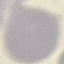
Summary:
  - Result: no malaria parasites detected
  - Image type: cell patch, automatically extracted from a larger field of view and resized to 64 × 64 pixels
  - Stain: Giemsa
  - Capture: smartphone through the microscope eyepiece
  - Preparation: thin blood smear